Identify the blood parasite species.
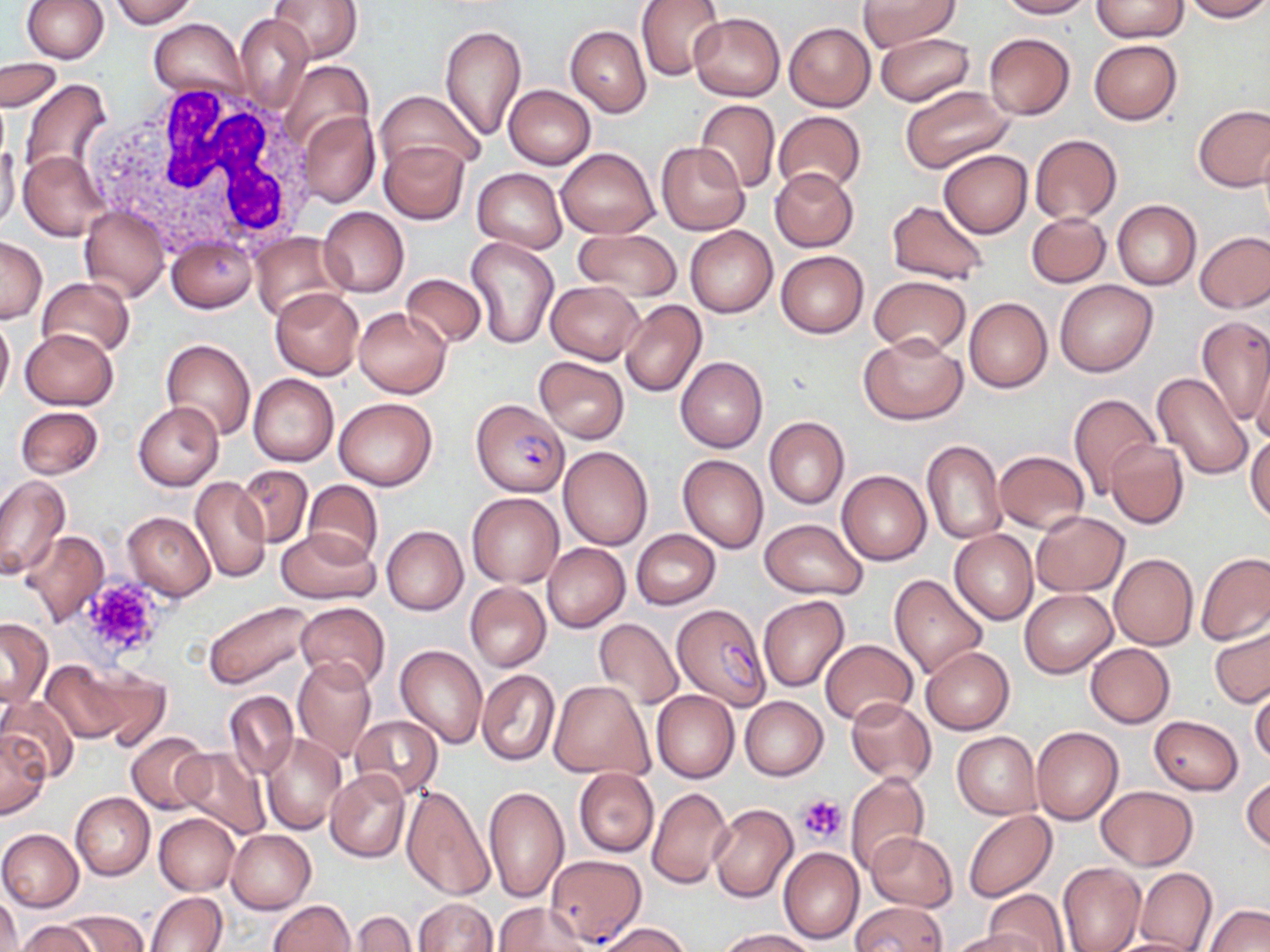

Plasmodium falciparum.

uninfected_red_blood_cell_locations_subset: 'approximate bounding boxes as named x1/y1/x2/y2 corners in pixels: (x1=22, y1=0, x2=109, y2=63), (x1=268, y1=0, x2=364, y2=65), (x1=636, y1=0, x2=725, y2=81), (x1=857, y1=0, x2=961, y2=50), (x1=995, y1=0, x2=1093, y2=19), (x1=1091, y1=0, x2=1187, y2=41), (x1=1180, y1=0, x2=1270, y2=22), (x1=110, y1=1, x2=196, y2=27), (x1=689, y1=12, x2=785, y2=101), (x1=234, y1=14, x2=312, y2=114), (x1=148, y1=19, x2=247, y2=100), (x1=784, y1=22, x2=875, y2=112), (x1=565, y1=25, x2=651, y2=117), (x1=439, y1=26, x2=527, y2=142), (x1=874, y1=32, x2=974, y2=106), (x1=983, y1=33, x2=1076, y2=120), (x1=1089, y1=39, x2=1183, y2=124), (x1=2, y1=59, x2=63, y2=112), (x1=279, y1=60, x2=373, y2=158), (x1=17, y1=80, x2=113, y2=186), (x1=503, y1=85, x2=596, y2=169), (x1=900, y1=86, x2=1016, y2=173), (x1=376, y1=90, x2=480, y2=183), (x1=694, y1=100, x2=780, y2=193), (x1=1192, y1=104, x2=1270, y2=192), (x1=298, y1=110, x2=380, y2=207), (x1=774, y1=111, x2=867, y2=195), (x1=1029, y1=134, x2=1123, y2=224), (x1=379, y1=140, x2=469, y2=225), (x1=656, y1=141, x2=750, y2=235), (x1=0, y1=143, x2=21, y2=232), (x1=556, y1=147, x2=659, y2=239), (x1=938, y1=149, x2=1032, y2=238), (x1=19, y1=150, x2=107, y2=240), (x1=769, y1=167, x2=858, y2=252), (x1=473, y1=168, x2=566, y2=254), (x1=886, y1=200, x2=990, y2=286), (x1=1112, y1=200, x2=1200, y2=289), (x1=80, y1=205, x2=169, y2=302), (x1=318, y1=208, x2=410, y2=296), (x1=1026, y1=212, x2=1111, y2=287), (x1=686, y1=226, x2=777, y2=317), (x1=573, y1=228, x2=682, y2=302), (x1=1195, y1=231, x2=1270, y2=313), (x1=246, y1=232, x2=346, y2=324), (x1=165, y1=233, x2=258, y2=312), (x1=0, y1=235, x2=47, y2=323), (x1=466, y1=236, x2=559, y2=349), (x1=776, y1=250, x2=868, y2=338), (x1=401, y1=273, x2=488, y2=348), (x1=870, y1=276, x2=971, y2=356), (x1=37, y1=278, x2=134, y2=359), (x1=1055, y1=279, x2=1157, y2=377), (x1=546, y1=281, x2=644, y2=363), (x1=271, y1=287, x2=364, y2=379), (x1=964, y1=298, x2=1052, y2=393), (x1=621, y1=301, x2=706, y2=397), (x1=354, y1=307, x2=450, y2=398), (x1=0, y1=315, x2=14, y2=405), (x1=1197, y1=315, x2=1270, y2=426), (x1=19, y1=328, x2=118, y2=410), (x1=860, y1=334, x2=967, y2=423), (x1=162, y1=339, x2=256, y2=440), (x1=534, y1=356, x2=629, y2=443), (x1=1249, y1=356, x2=1270, y2=449), (x1=675, y1=357, x2=768, y2=453), (x1=1150, y1=371, x2=1253, y2=479), (x1=248, y1=373, x2=339, y2=466), (x1=1068, y1=394, x2=1160, y2=496), (x1=333, y1=397, x2=438, y2=491), (x1=133, y1=401, x2=224, y2=490), (x1=16, y1=406, x2=103, y2=479), (x1=765, y1=417, x2=849, y2=508), (x1=1247, y1=432, x2=1270, y2=525), (x1=922, y1=439, x2=1005, y2=545), (x1=1105, y1=440, x2=1188, y2=529), (x1=559, y1=447, x2=653, y2=550), (x1=994, y1=451, x2=1088, y2=533), (x1=678, y1=455, x2=769, y2=552), (x1=235, y1=466, x2=313, y2=548), (x1=837, y1=469, x2=931, y2=565), (x1=190, y1=475, x2=270, y2=585), (x1=0, y1=477, x2=70, y2=579), (x1=303, y1=480, x2=384, y2=567), (x1=466, y1=492, x2=564, y2=588), (x1=1031, y1=510, x2=1128, y2=596), (x1=123, y1=512, x2=215, y2=600), (x1=759, y1=518, x2=868, y2=599), (x1=382, y1=526, x2=468, y2=614), (x1=277, y1=528, x2=377, y2=604), (x1=949, y1=528, x2=1038, y2=624), (x1=630, y1=529, x2=720, y2=608), (x1=20, y1=531, x2=110, y2=625), (x1=542, y1=542, x2=630, y2=632), (x1=1108, y1=553, x2=1198, y2=650), (x1=1196, y1=553, x2=1270, y2=645), (x1=889, y1=574, x2=988, y2=680), (x1=465, y1=583, x2=550, y2=671), (x1=1020, y1=589, x2=1116, y2=677), (x1=758, y1=595, x2=848, y2=692), (x1=203, y1=600, x2=318, y2=689), (x1=295, y1=602, x2=391, y2=691), (x1=0, y1=617, x2=53, y2=706), (x1=594, y1=619, x2=682, y2=709), (x1=1210, y1=624, x2=1269, y2=708), (x1=819, y1=639, x2=918, y2=725), (x1=1085, y1=643, x2=1175, y2=727), (x1=395, y1=645, x2=489, y2=748), (x1=920, y1=646, x2=1015, y2=734), (x1=292, y1=656, x2=377, y2=762), (x1=40, y1=660, x2=132, y2=743), (x1=85, y1=670, x2=170, y2=750), (x1=477, y1=670, x2=560, y2=765), (x1=549, y1=680, x2=653, y2=780), (x1=1250, y1=684, x2=1270, y2=765), (x1=652, y1=689, x2=740, y2=783), (x1=224, y1=690, x2=298, y2=780), (x1=739, y1=695, x2=828, y2=781), (x1=0, y1=696, x2=80, y2=784), (x1=846, y1=696, x2=935, y2=784), (x1=350, y1=714, x2=442, y2=801), (x1=1149, y1=716, x2=1243, y2=794), (x1=1031, y1=726, x2=1123, y2=824), (x1=0, y1=730, x2=50, y2=818), (x1=952, y1=731, x2=1041, y2=819), (x1=127, y1=732, x2=210, y2=813), (x1=262, y1=733, x2=348, y2=834), (x1=173, y1=748, x2=270, y2=837), (x1=573, y1=768, x2=658, y2=857), (x1=326, y1=769, x2=411, y2=862), (x1=845, y1=771, x2=929, y2=875), (x1=1242, y1=778, x2=1270, y2=855), (x1=400, y1=784, x2=494, y2=901), (x1=483, y1=785, x2=569, y2=903), (x1=646, y1=786, x2=733, y2=889), (x1=1096, y1=786, x2=1198, y2=871), (x1=71, y1=792, x2=155, y2=881), (x1=708, y1=804, x2=798, y2=903), (x1=963, y1=810, x2=1057, y2=901), (x1=154, y1=812, x2=239, y2=894), (x1=0, y1=828, x2=83, y2=912), (x1=227, y1=830, x2=316, y2=913), (x1=865, y1=831, x2=957, y2=911), (x1=778, y1=847, x2=864, y2=943), (x1=544, y1=854, x2=647, y2=946), (x1=1057, y1=862, x2=1146, y2=952), (x1=1134, y1=868, x2=1217, y2=952), (x1=984, y1=889, x2=1070, y2=952), (x1=146, y1=891, x2=229, y2=952), (x1=1, y1=893, x2=22, y2=952), (x1=412, y1=898, x2=497, y2=952), (x1=267, y1=900, x2=355, y2=952), (x1=852, y1=901, x2=947, y2=951), (x1=493, y1=902, x2=591, y2=951), (x1=1203, y1=904, x2=1269, y2=952), (x1=61, y1=909, x2=151, y2=951), (x1=349, y1=911, x2=418, y2=952), (x1=14, y1=920, x2=98, y2=952), (x1=594, y1=922, x2=694, y2=952), (x1=717, y1=928, x2=819, y2=951), (x1=947, y1=929, x2=1045, y2=952), (x1=1105, y1=937, x2=1208, y2=952)'
white_blood_cell_locations: 'approximate bounding boxes as named x1/y1/x2/y2 corners in pixels: (x1=92, y1=81, x2=320, y2=263)'
preparation: thin blood film
modality: light microscopy
platelet_locations: 'approximate bounding boxes as named x1/y1/x2/y2 corners in pixels: (x1=79, y1=576, x2=165, y2=661), (x1=798, y1=794, x2=846, y2=843)'
magnification: 1000x
plasmodium_falciparum_infected_red_blood_cell_locations_subset: 'approximate bounding boxes as named x1/y1/x2/y2 corners in pixels: (x1=472, y1=398, x2=570, y2=497)'
image_size: 1270×952 pixels
stain: May-Grünwald-Giemsa
field_of_view: one of a larger specimen